Locate every blood parasite and identify its species.
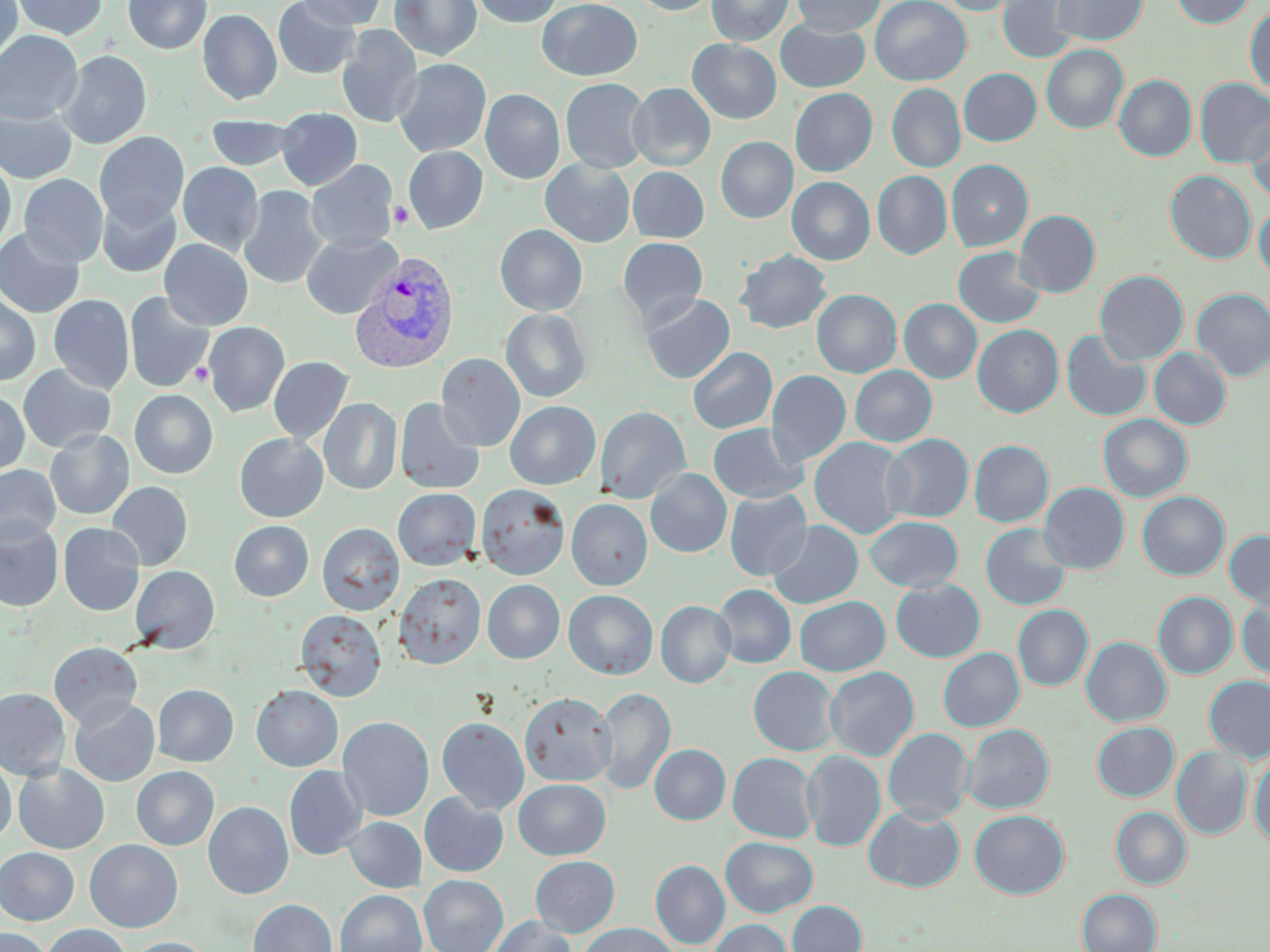

Approximate bounding boxes as [x1, y1, x2, y2] in pixels.
Plasmodium vivax-infected red blood cells: [350, 251, 459, 373].
No Plasmodium falciparum, Plasmodium ovale, Plasmodium malariae, Babesia divergens, or Trypanosoma brucei observed.

Summary:
  - Platelet locations: [389, 200, 415, 229], [191, 362, 212, 387]
  - Uninfected red blood cell locations: [0, 0, 22, 64], [11, 0, 107, 39], [123, 0, 212, 55], [272, 0, 361, 79], [296, 0, 385, 29], [390, 0, 482, 61], [470, 0, 562, 28], [537, 0, 642, 80], [631, 0, 719, 15], [707, 0, 793, 46], [792, 0, 885, 36], [870, 0, 971, 86], [936, 0, 1025, 16], [998, 0, 1080, 63], [1052, 0, 1148, 45], [1170, 0, 1255, 28], [1245, 5, 1270, 93], [198, 9, 282, 105], [775, 19, 870, 93], [336, 24, 422, 128], [0, 30, 82, 124], [687, 39, 781, 124], [1041, 45, 1128, 133], [57, 50, 151, 149], [393, 58, 491, 157], [959, 68, 1041, 146], [1114, 75, 1196, 161], [560, 78, 651, 174], [1195, 78, 1270, 167], [628, 83, 716, 171], [887, 83, 966, 172], [789, 88, 877, 177], [480, 89, 565, 184], [0, 102, 77, 184], [276, 108, 362, 190], [1245, 114, 1270, 204], [206, 116, 297, 171], [94, 131, 189, 228], [716, 136, 797, 223], [403, 146, 488, 234], [0, 158, 15, 253], [540, 158, 635, 247], [946, 159, 1033, 251], [306, 160, 397, 253], [178, 162, 263, 256], [628, 167, 709, 243], [1165, 170, 1256, 264], [872, 171, 952, 259], [19, 173, 107, 267], [787, 177, 874, 265], [237, 186, 328, 290], [97, 194, 181, 278], [1254, 204, 1270, 281], [1014, 210, 1100, 297], [495, 224, 587, 316], [0, 227, 85, 318], [301, 232, 402, 319], [617, 237, 708, 327], [159, 239, 253, 331], [952, 246, 1045, 329], [735, 250, 831, 334], [1094, 270, 1189, 365], [1192, 288, 1270, 381], [811, 289, 902, 378], [124, 292, 214, 392], [640, 293, 735, 384], [0, 294, 40, 386], [48, 294, 134, 394], [899, 298, 982, 384], [500, 308, 591, 403], [203, 322, 289, 416], [972, 324, 1063, 417], [1061, 330, 1151, 421], [687, 347, 777, 434], [1149, 348, 1231, 430], [436, 353, 525, 451], [268, 356, 353, 445], [18, 364, 116, 453], [850, 365, 937, 446], [766, 370, 851, 465], [129, 390, 218, 478], [0, 391, 30, 476], [318, 397, 402, 495], [394, 398, 485, 495], [505, 401, 600, 490], [595, 405, 691, 503], [1098, 414, 1192, 502], [708, 423, 808, 504], [45, 429, 133, 519], [234, 433, 328, 522], [882, 434, 973, 523], [809, 437, 911, 539], [969, 440, 1053, 527], [0, 464, 60, 546], [645, 468, 732, 557], [107, 481, 193, 570], [1039, 482, 1129, 574], [476, 484, 570, 580], [393, 488, 481, 570], [725, 490, 812, 581], [1137, 491, 1229, 580], [566, 498, 652, 590], [865, 516, 963, 592], [0, 519, 63, 612], [229, 520, 314, 601], [767, 520, 863, 608], [58, 523, 145, 615], [317, 523, 404, 615], [980, 523, 1071, 610], [1224, 530, 1270, 612], [129, 565, 220, 653], [394, 573, 485, 669], [891, 578, 985, 662], [482, 580, 564, 663], [712, 584, 796, 668], [564, 590, 658, 679], [1153, 592, 1238, 679], [795, 596, 890, 676], [1236, 597, 1270, 682], [656, 600, 735, 688], [1012, 605, 1093, 691], [295, 609, 386, 701], [1081, 637, 1171, 727], [48, 642, 142, 729], [938, 647, 1024, 731], [748, 666, 840, 756], [824, 666, 919, 761], [1203, 676, 1270, 764], [153, 684, 238, 766], [251, 685, 343, 772], [0, 687, 71, 780], [592, 687, 676, 796], [7, 688, 88, 854], [519, 692, 616, 786], [69, 697, 160, 787], [338, 717, 434, 821], [436, 717, 529, 814], [1091, 722, 1179, 801], [962, 724, 1054, 814], [883, 728, 973, 823], [649, 744, 730, 825], [1172, 746, 1253, 840], [802, 749, 886, 852], [727, 752, 819, 843], [1249, 753, 1270, 847], [0, 759, 16, 846], [13, 763, 109, 854], [284, 765, 368, 860], [131, 766, 219, 850], [513, 779, 611, 859], [419, 793, 509, 877], [203, 802, 293, 899], [864, 805, 964, 893], [1111, 807, 1191, 888], [970, 810, 1069, 898], [344, 817, 426, 893], [721, 837, 818, 917], [84, 839, 183, 932], [0, 848, 79, 925], [530, 855, 620, 937], [651, 860, 730, 949], [419, 875, 508, 952], [1077, 888, 1162, 952], [335, 890, 426, 952], [247, 899, 337, 952], [787, 900, 867, 952], [489, 916, 576, 952], [708, 919, 793, 952], [579, 923, 680, 952], [43, 924, 130, 952], [0, 927, 51, 952], [126, 937, 214, 952]
  - Slide-level diagnosis: Plasmodium vivax
  - Stain: May-Grünwald-Giemsa
  - Image size: 1270×952 pixels
  - Field of view: one of a larger specimen
  - Modality: light microscopy
  - Preparation: thin blood film
  - Magnification: 1000x